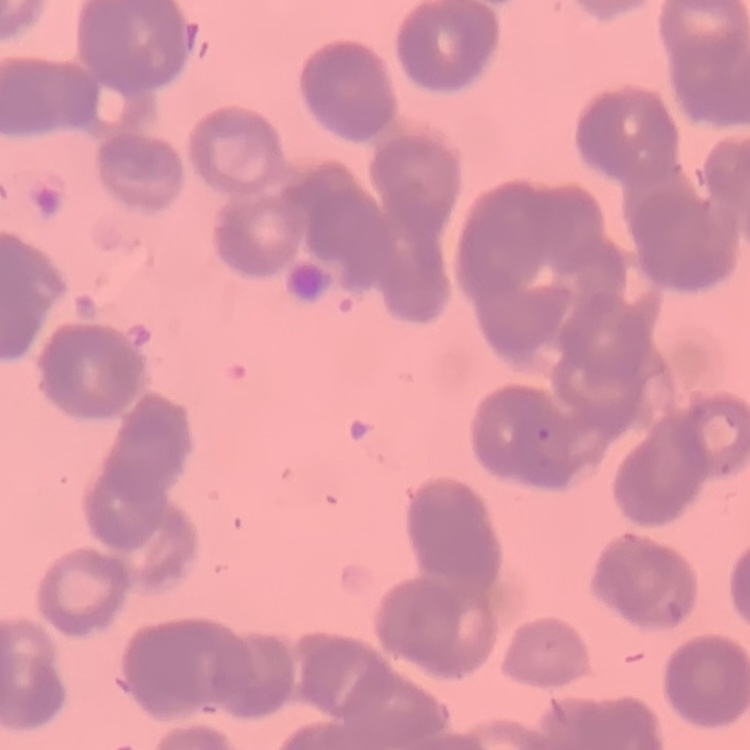
{
  "red_blood_cell_morphology": "rouleaux formation",
  "preparation": "thin blood smear",
  "stain": "Field's or Giemsa",
  "image_type": "one tile cut from a larger photomicrograph"
}